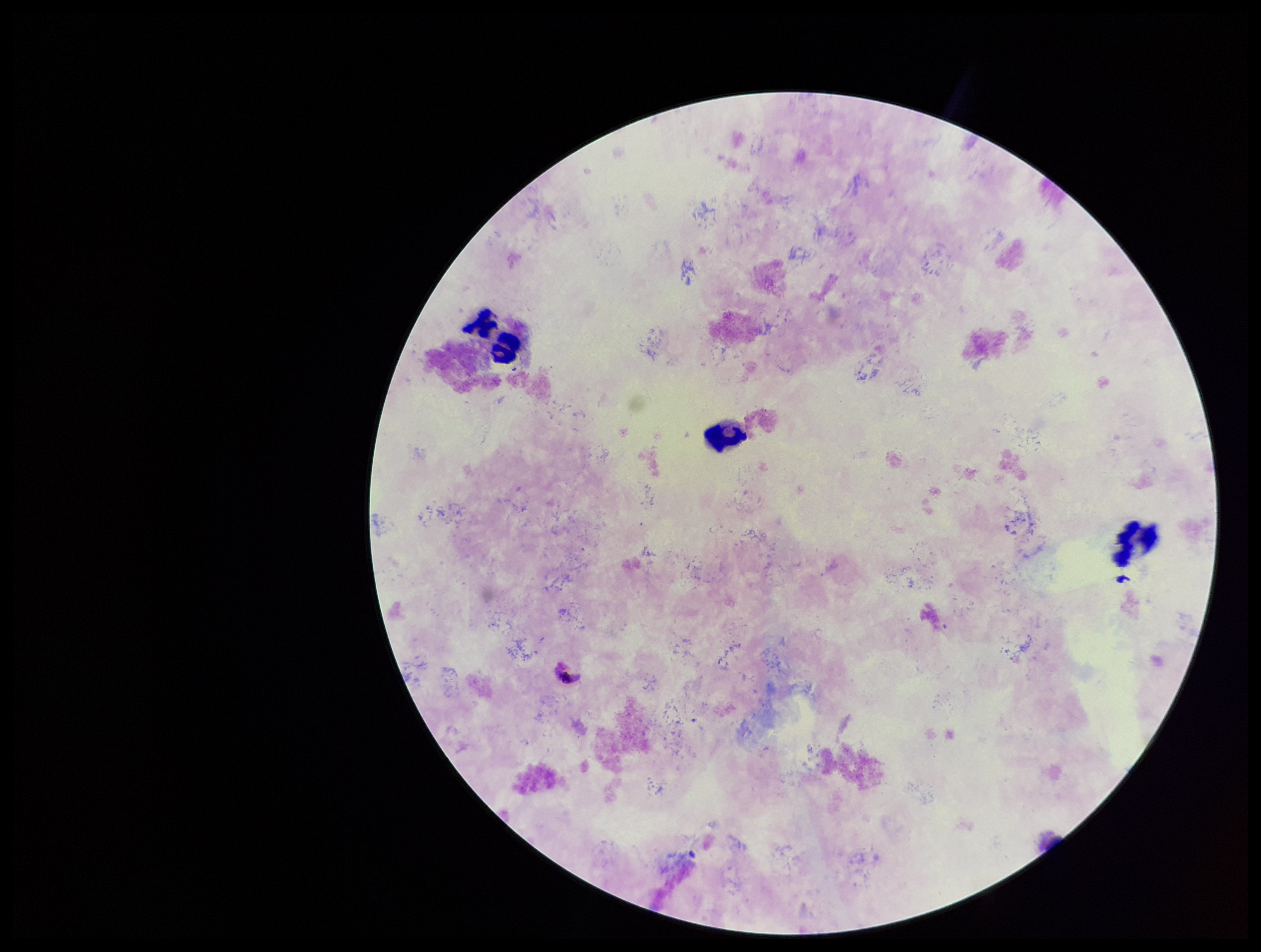
parasite count = 0
field of view = one from this slide
image size = 1261×952 pixels
species reported for this patient = Plasmodium falciparum
stain = Giemsa
patient malaria status = positive
preparation = thick blood smear
Plasmodium parasites = none identified
capture = smartphone photograph through the microscope eyepiece
leukocyte count = 4